Classify this cell by malaria status.
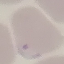

It is parasitized.

capture = smartphone camera at the microscope eyepiece
preparation = thin blood film
image type = cell patch, automatically extracted from a larger field of view and resized to 64 × 64 pixels
stain = Giemsa